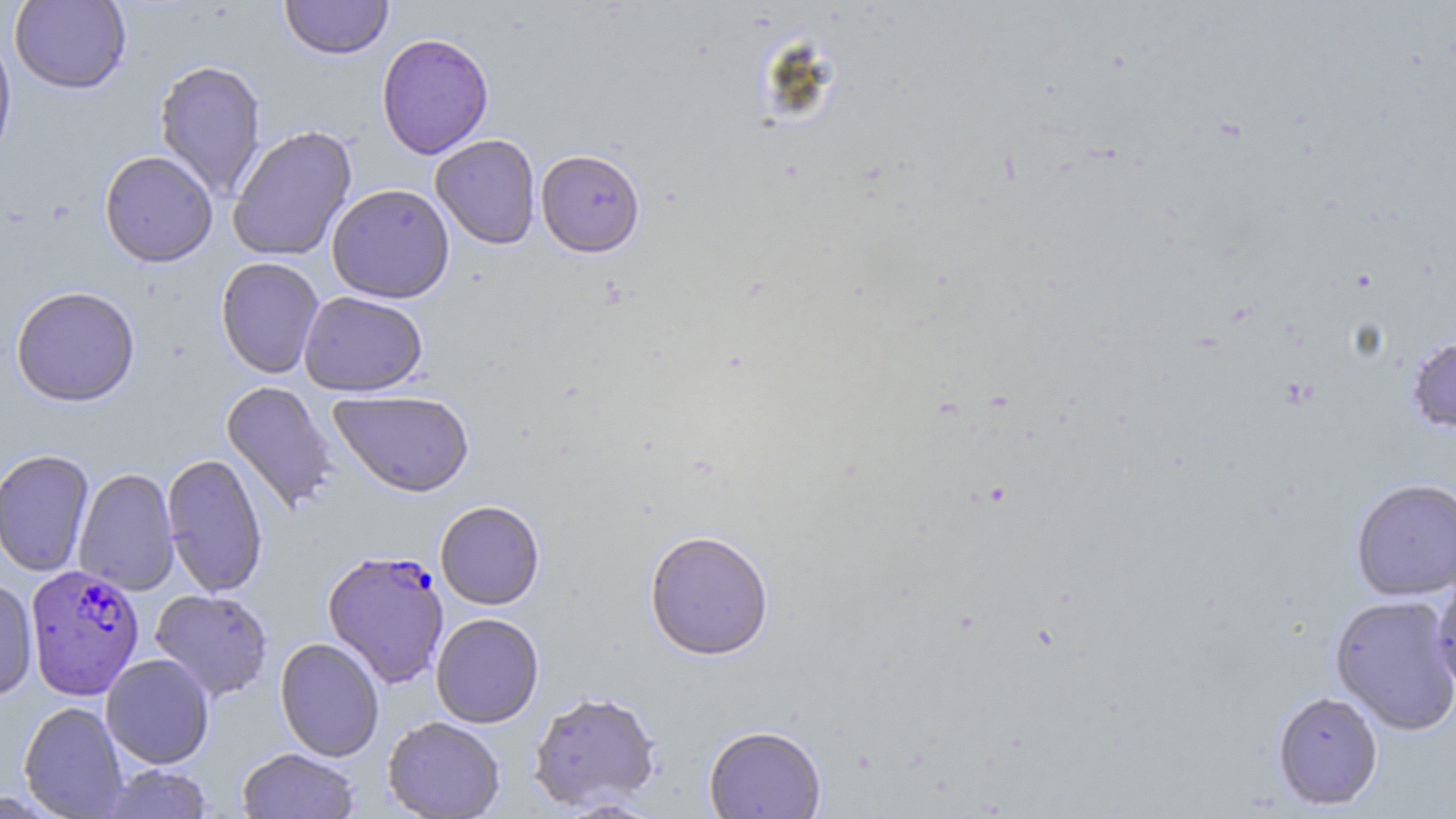

Approximate bounding boxes as (x1,y1)-(x2,y2) corner pairs in pixels. Uninfected red blood cell locations: (279,0)-(393,60), (9,1)-(131,95), (0,30)-(17,167), (376,32)-(494,160), (153,59)-(267,200), (227,125)-(357,261), (430,134)-(541,250), (536,149)-(646,258), (99,150)-(218,268), (326,184)-(455,303), (215,257)-(325,379), (11,285)-(141,407), (299,291)-(428,397), (1406,335)-(1456,433), (220,381)-(339,517), (329,389)-(475,497), (0,448)-(94,577), (162,452)-(268,598), (73,467)-(179,596), (1350,478)-(1456,600), (435,500)-(545,610), (643,529)-(775,661), (1430,573)-(1456,696), (0,577)-(38,703), (150,588)-(274,702), (1330,594)-(1456,735), (431,613)-(544,728), (275,637)-(385,761), (100,653)-(214,768), (528,690)-(662,812), (1271,690)-(1384,810), (19,701)-(129,818), (382,716)-(506,819), (704,724)-(826,819), (237,747)-(360,819), (99,764)-(214,819). Plasmodium falciparum-infected red blood cell locations: (322,550)-(450,688), (25,564)-(145,700). Slide-level diagnosis: Plasmodium falciparum. Thin blood smear. May-Grünwald-Giemsa stain. Light microscopy. Image is 1456×819 pixels. 1000x magnification. One field of a larger specimen.